Classify this cell by malaria status.
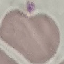

It is uninfected.

Giemsa stain. Cell patch, automatically extracted from a larger field of view and resized to 64 × 64 pixels. Photographed with a smartphone camera at the microscope eyepiece. Thin blood smear.